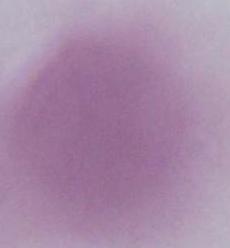

Micrograph. A red blood cell is shown. 1000x magnification.